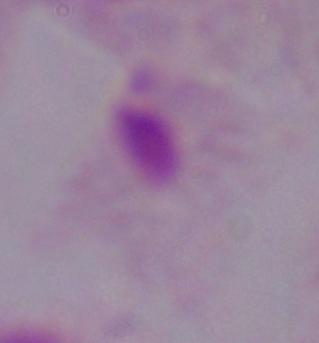
1000x magnification. A trichomonad is seen. Photomicrograph.